Outline each Babesia divergens-infected red blood cell.
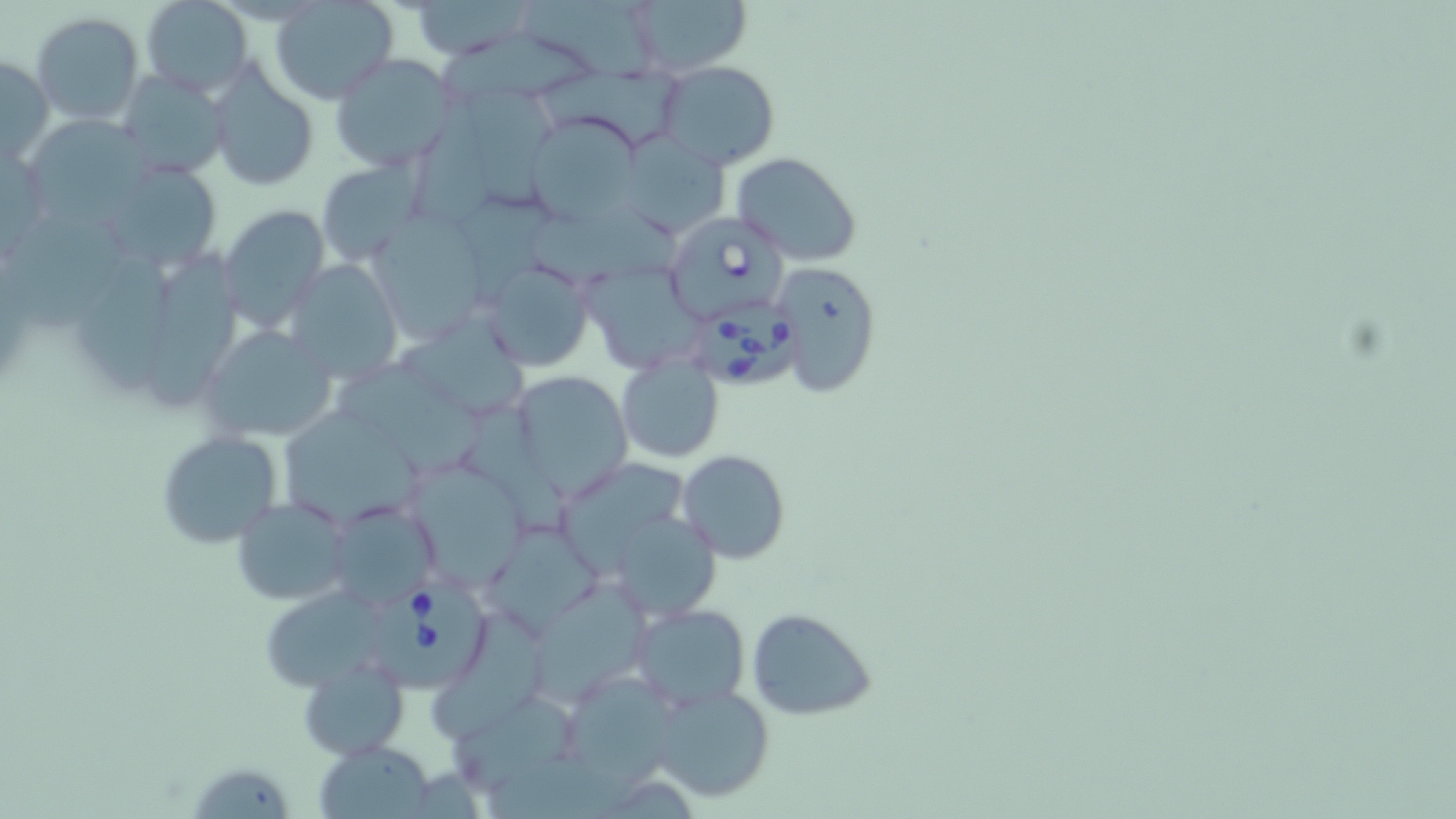
Approximate bounding boxes as named x1/y1/x2/y2 corners in pixels.
Babesia divergens-infected red blood cells: (x1=661, y1=211, x2=790, y2=321), (x1=690, y1=303, x2=814, y2=394), (x1=365, y1=581, x2=496, y2=689).

Summary:
  - Uninfected red blood cell locations: (x1=141, y1=0, x2=253, y2=97), (x1=407, y1=0, x2=539, y2=60), (x1=524, y1=0, x2=658, y2=92), (x1=625, y1=0, x2=755, y2=77), (x1=270, y1=1, x2=399, y2=103), (x1=31, y1=13, x2=144, y2=126), (x1=442, y1=36, x2=595, y2=98), (x1=329, y1=53, x2=458, y2=172), (x1=0, y1=55, x2=53, y2=165), (x1=658, y1=60, x2=781, y2=170), (x1=538, y1=63, x2=684, y2=142), (x1=206, y1=65, x2=320, y2=191), (x1=115, y1=71, x2=228, y2=179), (x1=464, y1=79, x2=559, y2=209), (x1=412, y1=102, x2=508, y2=247), (x1=29, y1=112, x2=150, y2=227), (x1=527, y1=114, x2=644, y2=225), (x1=613, y1=134, x2=733, y2=239), (x1=729, y1=152, x2=863, y2=267), (x1=96, y1=159, x2=224, y2=270), (x1=315, y1=159, x2=424, y2=264), (x1=458, y1=194, x2=556, y2=311), (x1=218, y1=203, x2=328, y2=334), (x1=11, y1=210, x2=127, y2=342), (x1=531, y1=212, x2=677, y2=286), (x1=375, y1=218, x2=493, y2=353), (x1=79, y1=251, x2=173, y2=401), (x1=148, y1=251, x2=240, y2=410), (x1=283, y1=259, x2=400, y2=381), (x1=481, y1=260, x2=596, y2=372), (x1=772, y1=260, x2=882, y2=399), (x1=587, y1=273, x2=708, y2=381), (x1=398, y1=315, x2=531, y2=416), (x1=199, y1=325, x2=341, y2=444), (x1=615, y1=355, x2=724, y2=462), (x1=342, y1=363, x2=481, y2=476), (x1=507, y1=370, x2=631, y2=498), (x1=286, y1=407, x2=426, y2=521), (x1=462, y1=413, x2=580, y2=543), (x1=155, y1=431, x2=282, y2=550), (x1=677, y1=450, x2=788, y2=563), (x1=404, y1=460, x2=528, y2=588), (x1=233, y1=496, x2=351, y2=605), (x1=324, y1=499, x2=442, y2=613), (x1=605, y1=510, x2=723, y2=621), (x1=482, y1=522, x2=601, y2=636), (x1=535, y1=585, x2=663, y2=703), (x1=260, y1=596, x2=381, y2=693), (x1=630, y1=604, x2=751, y2=713), (x1=746, y1=608, x2=878, y2=719), (x1=433, y1=612, x2=550, y2=738), (x1=299, y1=654, x2=410, y2=761), (x1=572, y1=682, x2=684, y2=790), (x1=648, y1=682, x2=773, y2=803), (x1=452, y1=691, x2=584, y2=796), (x1=316, y1=740, x2=436, y2=817), (x1=190, y1=760, x2=287, y2=819)
  - Slide-level diagnosis: Babesia divergens
  - Preparation: thin blood smear
  - Modality: optical microscopy
  - Magnification: 1000x
  - Image size: 1456×819 pixels
  - Field of view: single
  - Stain: May-Grünwald-Giemsa